Identify the blood parasite species.
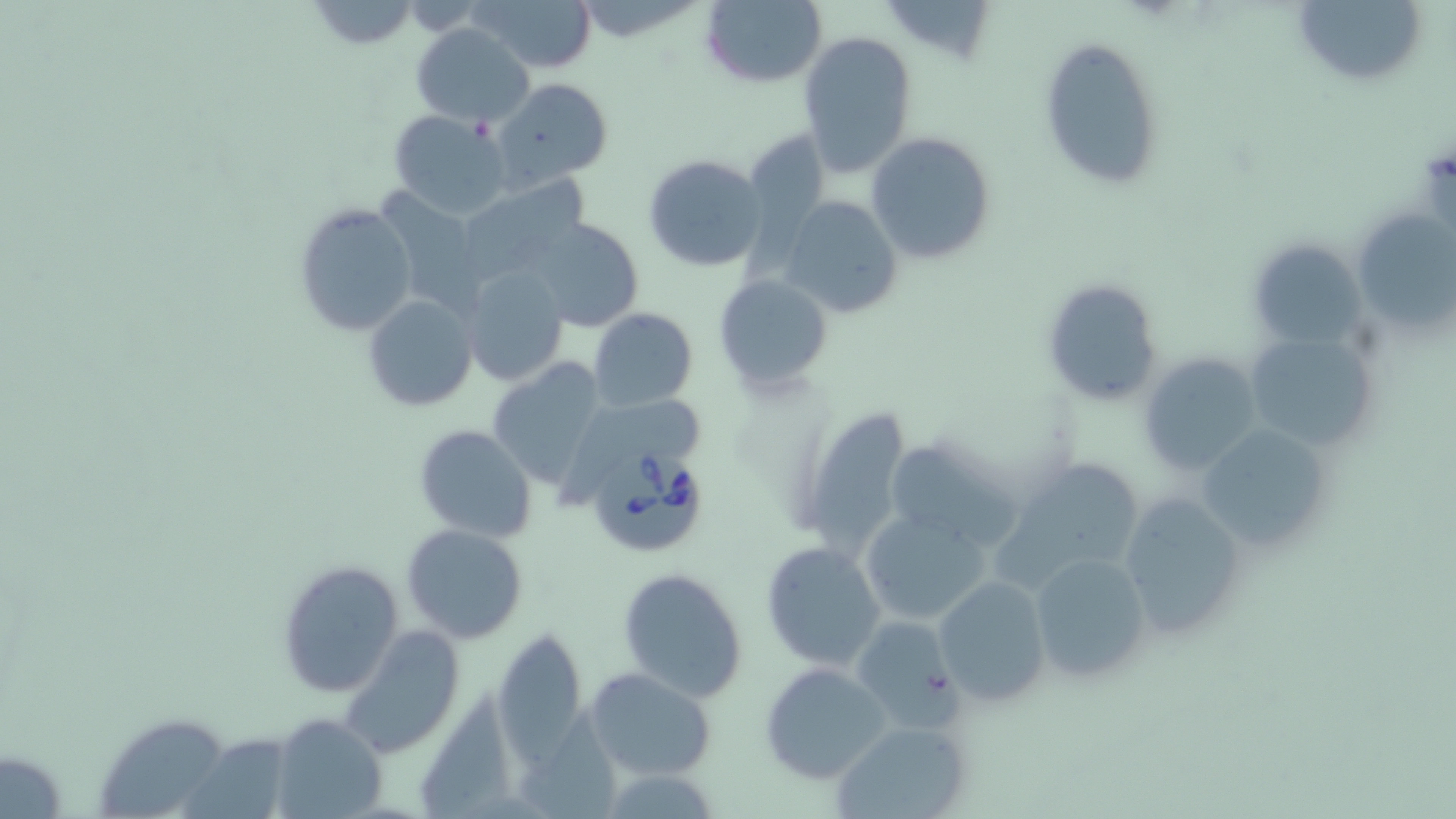

Babesia divergens.

Summary:
  - Coordinate format: approximate bounding boxes as [x1, y1, x2, y2] in pixels
  - Babesia divergens-infected red blood cell locations: [584, 444, 710, 560]
  - Uninfected red blood cell locations: [474, 0, 600, 73], [697, 0, 827, 90], [1294, 0, 1425, 86], [305, 1, 419, 48], [411, 22, 534, 128], [1039, 34, 1164, 187], [799, 36, 917, 175], [487, 75, 615, 192], [389, 109, 512, 218], [867, 130, 996, 266], [644, 155, 767, 272], [454, 175, 596, 282], [780, 196, 903, 317], [295, 201, 418, 338], [1358, 211, 1456, 329], [523, 216, 644, 331], [1247, 237, 1364, 350], [460, 264, 571, 387], [716, 273, 832, 396], [1041, 278, 1163, 408], [362, 293, 479, 413], [589, 307, 697, 411], [1244, 334, 1379, 453], [1139, 355, 1261, 476], [492, 359, 608, 481], [794, 404, 918, 554], [1194, 421, 1335, 558], [413, 423, 539, 542], [884, 435, 1027, 553], [1002, 456, 1148, 582], [1116, 488, 1248, 642], [857, 509, 995, 626], [401, 524, 528, 643], [761, 542, 886, 669], [1027, 550, 1152, 685], [278, 560, 405, 696], [617, 566, 748, 703], [935, 575, 1051, 706], [848, 615, 959, 730], [339, 626, 465, 759], [494, 628, 591, 761], [759, 664, 891, 783], [584, 668, 716, 780], [425, 687, 524, 818], [516, 705, 635, 819], [272, 712, 387, 819], [102, 721, 227, 817], [830, 721, 970, 819], [183, 731, 305, 819]
  - Image size: 1456×819 pixels
  - Modality: light microscopy
  - Magnification: 1000x
  - Preparation: thin blood smear
  - Stain: May-Grünwald-Giemsa
  - Field of view: single